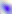
Summary:
  - Magnification: 400x
  - Modality: photomicrograph
  - Identification: Toxoplasma gondii